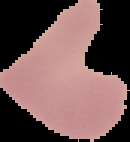

Summary:
  - Malaria status: uninfected
  - Preparation: thin blood smear
  - Image size: 130×142 pixels
  - Image type: segmented cell region on a black background